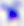 Toxoplasma gondii is shown. Micrograph. 400x magnification.